Classify this cell by malaria status.
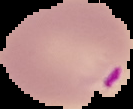

Parasitized.

The area outside the segmented cell region is set to black. Image is 133×109 pixels. From a thin blood film.